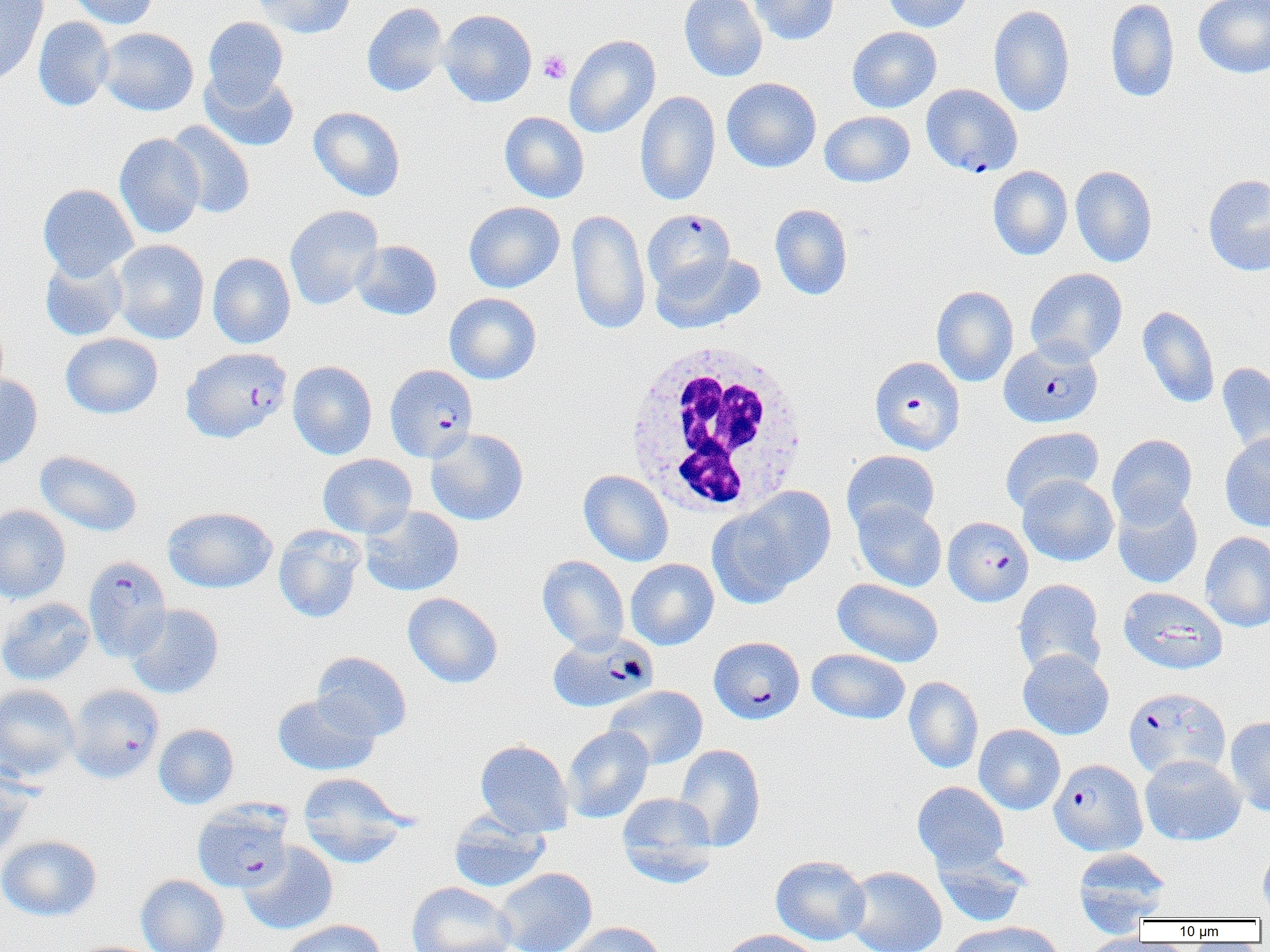
Approximate bounding boxes as (x1, y1, x2, y2) in pixels. White blood cell locations: (624, 336, 814, 512). Platelet locations: (539, 50, 571, 84). Plasmodium falciparum-infected red blood cell locations: (921, 83, 1022, 177), (643, 210, 736, 295), (999, 339, 1102, 428), (184, 347, 294, 443), (869, 356, 965, 456), (385, 364, 478, 462), (943, 516, 1033, 606), (83, 556, 172, 661), (547, 633, 658, 713), (708, 636, 805, 724), (66, 687, 163, 785), (1124, 688, 1231, 780), (1049, 759, 1147, 855), (192, 801, 293, 892). Uninfected red blood cell locations: (0, 0, 48, 86), (67, 0, 159, 29), (251, 0, 357, 38), (679, 0, 768, 82), (749, 0, 839, 45), (881, 0, 974, 32), (1105, 0, 1179, 104), (1193, 0, 1270, 79), (361, 2, 449, 97), (989, 5, 1075, 117), (439, 9, 537, 108), (33, 16, 115, 112), (202, 17, 288, 105), (847, 26, 942, 113), (98, 27, 199, 116), (564, 34, 660, 139), (200, 70, 299, 152), (722, 77, 821, 172), (635, 91, 720, 206), (308, 106, 406, 202), (499, 111, 589, 203), (819, 111, 915, 187), (166, 121, 255, 219), (114, 133, 205, 238), (987, 165, 1073, 260), (1070, 165, 1157, 267), (1203, 174, 1270, 276), (38, 183, 139, 280), (464, 201, 565, 293), (770, 203, 853, 300), (284, 205, 383, 310), (567, 208, 650, 335), (111, 239, 209, 344), (351, 240, 442, 320), (208, 252, 295, 349), (650, 252, 764, 333), (39, 254, 128, 341), (1025, 268, 1127, 365), (931, 285, 1018, 387), (444, 292, 541, 384), (1138, 306, 1220, 408), (60, 333, 162, 419), (287, 360, 377, 460), (1216, 361, 1270, 459), (0, 374, 42, 471), (1000, 426, 1104, 513), (425, 428, 529, 526), (1107, 433, 1197, 525), (1220, 433, 1270, 532), (35, 450, 142, 537), (841, 450, 940, 536), (317, 453, 417, 538), (579, 470, 674, 567), (1018, 474, 1118, 566), (709, 487, 835, 606), (1112, 492, 1203, 589), (852, 501, 946, 592), (0, 504, 71, 604), (360, 505, 464, 597), (163, 506, 277, 593), (273, 525, 365, 623), (1200, 532, 1270, 632), (537, 555, 630, 653), (625, 558, 718, 650), (832, 578, 943, 667), (1013, 580, 1106, 678), (1119, 587, 1227, 675), (402, 592, 503, 688), (0, 597, 94, 686), (126, 603, 224, 698), (807, 648, 910, 725), (1017, 649, 1115, 740), (312, 652, 412, 741), (904, 676, 983, 774), (0, 683, 80, 782), (604, 685, 707, 770), (272, 692, 380, 776), (1225, 716, 1270, 817), (153, 723, 239, 809), (974, 724, 1065, 815), (562, 725, 653, 823), (475, 739, 574, 837), (674, 743, 766, 851), (1139, 754, 1245, 845), (0, 769, 35, 863), (298, 773, 410, 867), (912, 781, 1009, 871), (617, 792, 718, 885), (449, 811, 550, 893), (0, 834, 102, 921), (239, 842, 338, 935), (1258, 845, 1270, 915), (933, 848, 1032, 929), (1073, 848, 1171, 932), (770, 855, 871, 945), (845, 865, 947, 952), (495, 867, 598, 952), (135, 874, 229, 952), (406, 881, 516, 952), (278, 919, 385, 952), (946, 920, 1070, 952), (565, 921, 666, 952), (717, 929, 824, 952), (1079, 934, 1167, 952). Slide-level diagnosis: Plasmodium falciparum. Optical microscopy. Single field of view. Thin blood film. Captured at 1000x magnification. Image is 1270×952 pixels.